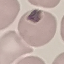

Result: negative for malaria parasites. Acquired by smartphone through the microscope eyepiece. Automatically extracted cell patch, resized to 64 × 64 pixels. Giemsa stain. Thin blood smear.